Give a bounding box for every malaria parasite, every leukocyte, and every artifact (stain precipitate or debris).
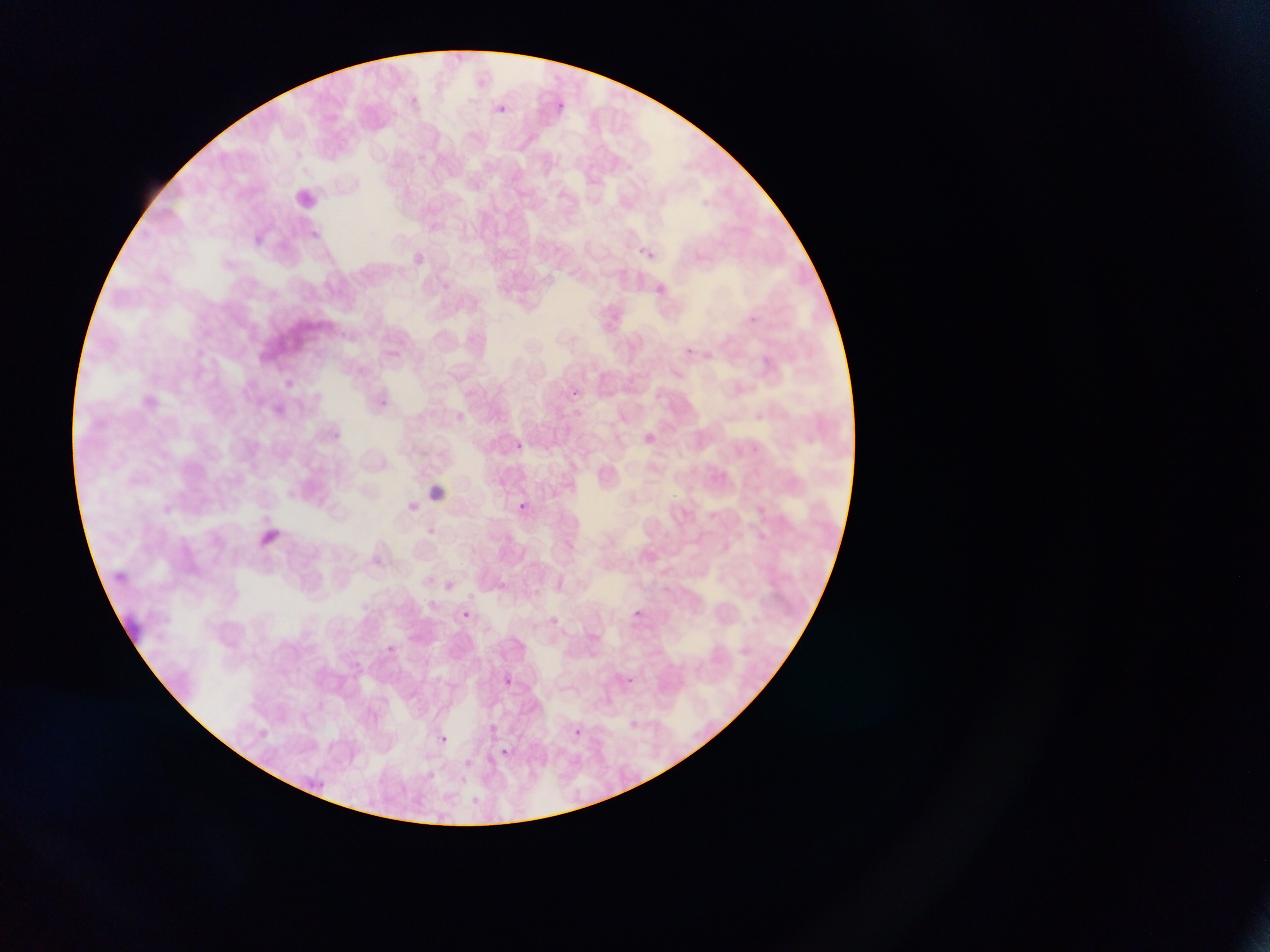
Approximate bounding boxes as {left, top, right, bottom} in pixels.
Malaria parasites: {552, 98, 583, 119}, {485, 102, 510, 117}, {249, 228, 276, 249}, {639, 241, 664, 265}, {746, 312, 761, 327}, {275, 367, 298, 387}, {567, 385, 588, 405}, {372, 388, 394, 410}, {510, 440, 524, 453}, {511, 499, 529, 515}, {426, 519, 441, 541}, {630, 607, 645, 621}, {457, 608, 470, 621}, {461, 610, 470, 618}, {383, 642, 414, 663}, {497, 673, 521, 691}, {570, 725, 585, 739}, {432, 730, 452, 748}, {494, 744, 515, 762}.
No leukocytes observed.

preparation: thin blood film
country: Ghana
capture: mobile-phone photograph through a microscope
field_of_view: single
image_size: 1270×952 pixels